Report the malaria status of this cell.
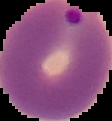
It is parasitized.

preparation: thin blood film
image_size: 112×121 pixels
image_type: cell region segmented out of the field of view; surrounding area masked to black